Identify the parasite.
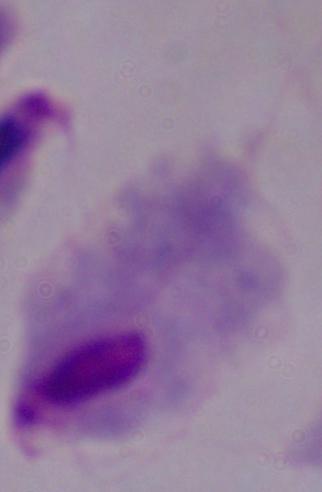

This is a trichomonad.

Photomicrograph. 1000x magnification.